State the blood parasite species.
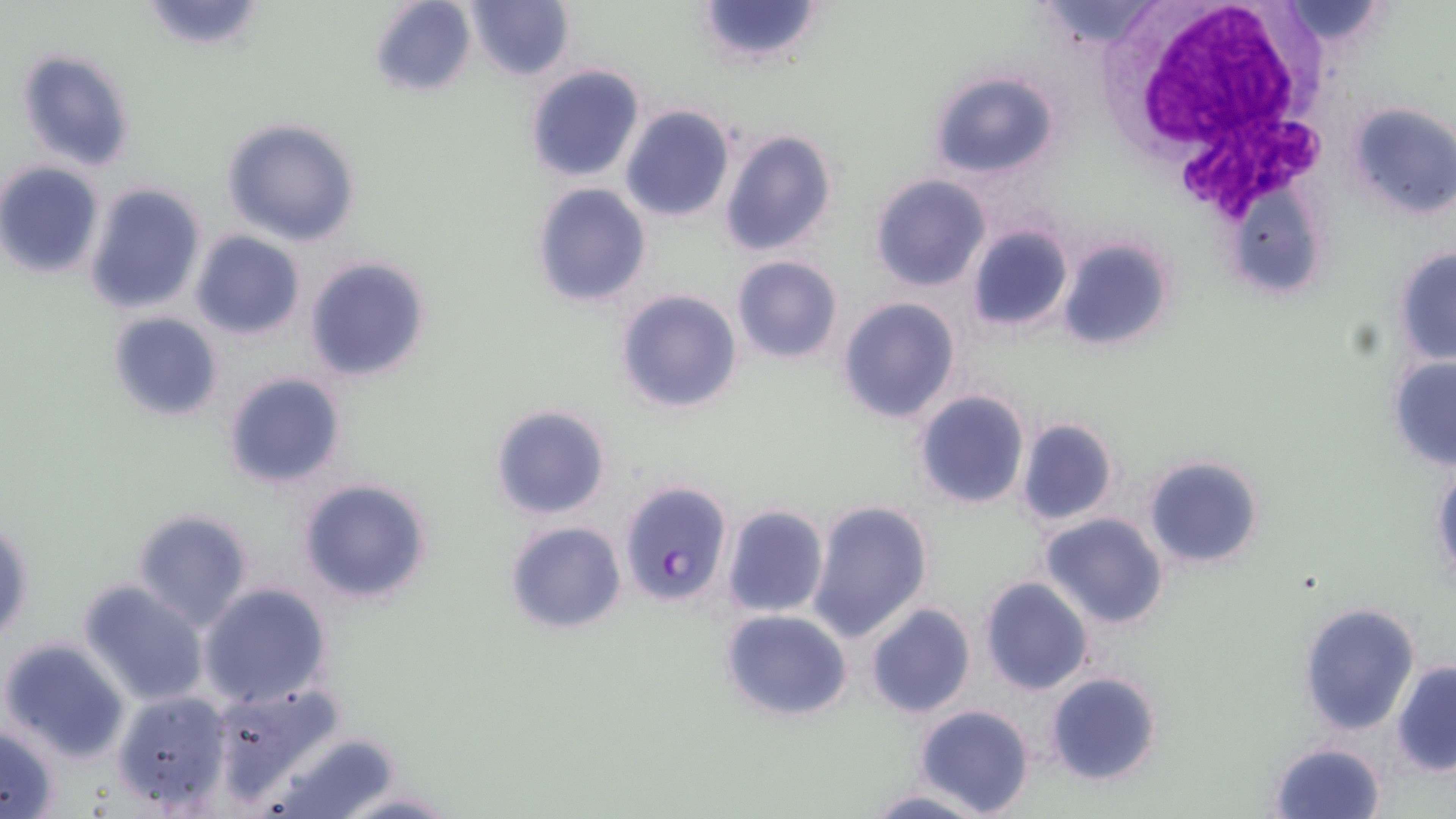

Plasmodium falciparum.

Approximate bounding boxes as named x1/y1/x2/y2 corners in pixels. White blood cell locations: (x1=1124, y1=0, x2=1331, y2=210). Plasmodium falciparum-infected red blood cell locations: (x1=619, y1=480, x2=733, y2=605). Uninfected red blood cell locations: (x1=135, y1=0, x2=269, y2=53), (x1=368, y1=0, x2=477, y2=97), (x1=692, y1=0, x2=825, y2=67), (x1=1032, y1=0, x2=1170, y2=53), (x1=464, y1=1, x2=573, y2=81), (x1=13, y1=47, x2=138, y2=172), (x1=524, y1=64, x2=646, y2=184), (x1=928, y1=69, x2=1060, y2=181), (x1=1347, y1=101, x2=1456, y2=222), (x1=620, y1=104, x2=736, y2=223), (x1=222, y1=119, x2=363, y2=246), (x1=719, y1=129, x2=836, y2=257), (x1=0, y1=162, x2=104, y2=279), (x1=871, y1=174, x2=991, y2=291), (x1=1229, y1=181, x2=1332, y2=298), (x1=83, y1=182, x2=207, y2=316), (x1=531, y1=183, x2=652, y2=307), (x1=966, y1=224, x2=1073, y2=332), (x1=191, y1=231, x2=306, y2=340), (x1=1057, y1=238, x2=1174, y2=352), (x1=1393, y1=248, x2=1456, y2=365), (x1=303, y1=256, x2=432, y2=383), (x1=731, y1=256, x2=844, y2=364), (x1=615, y1=289, x2=743, y2=413), (x1=836, y1=297, x2=961, y2=425), (x1=107, y1=311, x2=224, y2=424), (x1=1388, y1=356, x2=1456, y2=471), (x1=223, y1=372, x2=347, y2=490), (x1=914, y1=388, x2=1031, y2=511), (x1=490, y1=403, x2=611, y2=520), (x1=1015, y1=416, x2=1121, y2=526), (x1=1142, y1=456, x2=1265, y2=570), (x1=1431, y1=466, x2=1456, y2=584), (x1=297, y1=478, x2=434, y2=605), (x1=806, y1=499, x2=934, y2=644), (x1=723, y1=503, x2=829, y2=619), (x1=131, y1=508, x2=254, y2=632), (x1=1039, y1=512, x2=1169, y2=628), (x1=0, y1=518, x2=34, y2=650), (x1=505, y1=521, x2=627, y2=635), (x1=979, y1=576, x2=1094, y2=696), (x1=77, y1=581, x2=209, y2=707), (x1=198, y1=583, x2=332, y2=708), (x1=1298, y1=602, x2=1421, y2=736), (x1=865, y1=603, x2=976, y2=718), (x1=720, y1=609, x2=853, y2=722), (x1=1, y1=638, x2=132, y2=763), (x1=1391, y1=660, x2=1455, y2=776), (x1=1045, y1=669, x2=1162, y2=787), (x1=206, y1=678, x2=344, y2=804), (x1=110, y1=688, x2=232, y2=812), (x1=914, y1=704, x2=1035, y2=817), (x1=0, y1=725, x2=61, y2=817), (x1=271, y1=731, x2=402, y2=819), (x1=1266, y1=741, x2=1387, y2=819), (x1=332, y1=789, x2=458, y2=818), (x1=862, y1=789, x2=988, y2=819). 1000x magnification. Light microscopy. May-Grünwald-Giemsa-stained preparation. Thin blood film. One field of a larger specimen. Image is 1456×819 pixels.